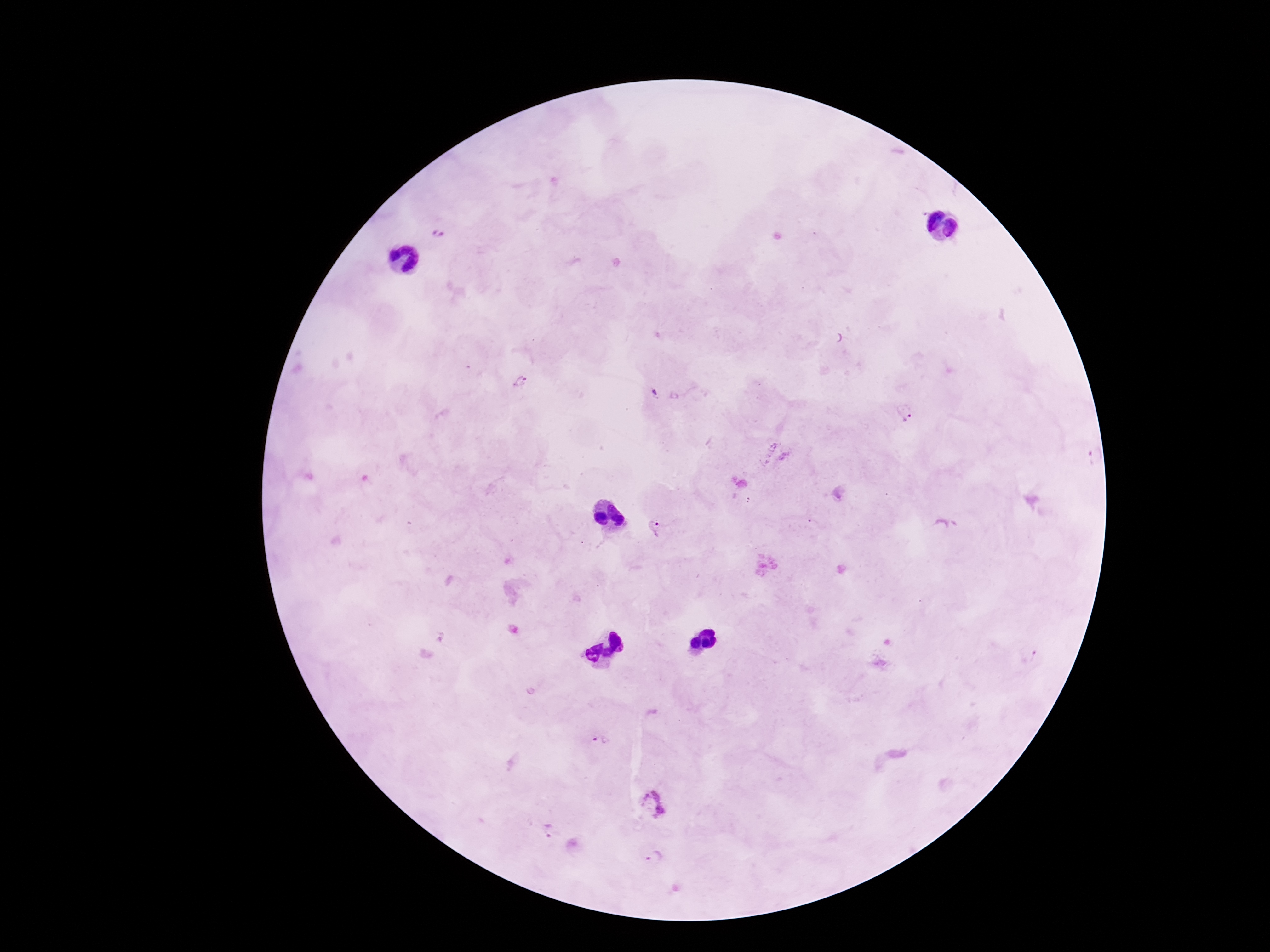

capture = smartphone camera through the microscope eyepiece
preparation = thick blood smear
Plasmodium parasite locations = approximate object centers, in pixels from the top-left corner: (x=438, y=233), (x=520, y=383), (x=905, y=413), (x=772, y=446), (x=783, y=457), (x=1089, y=457), (x=655, y=529), (x=598, y=743), (x=652, y=806), (x=547, y=829), (x=655, y=858)
image size = 1270×952 pixels
patient malaria status = infected
magnification = 100x
field of view = one from this slide
stain = Giemsa